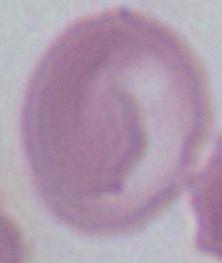

Micrograph. A red blood cell is seen. Captured at 1000x magnification.